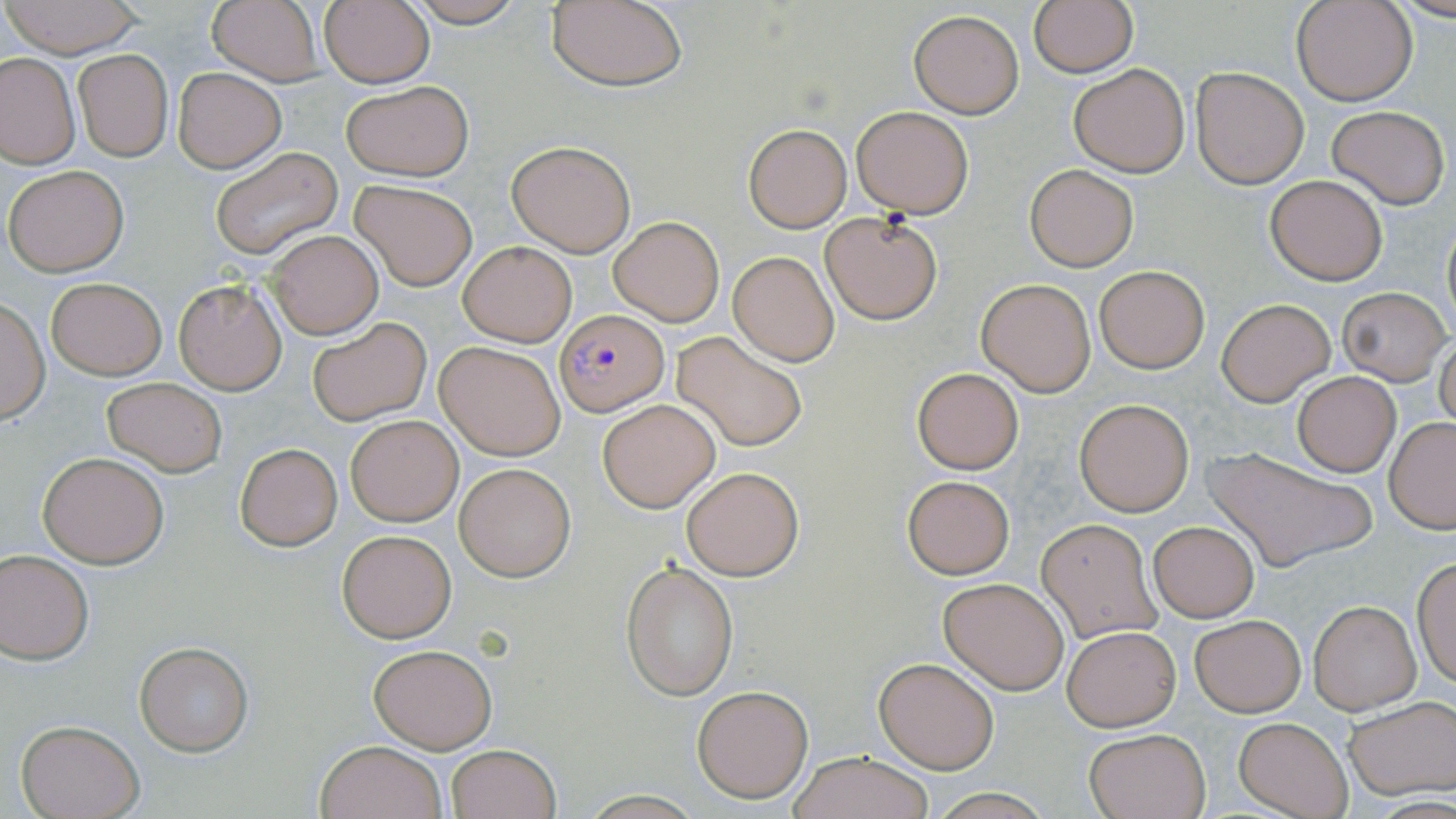
Approximate bounding boxes as named x1/y1/x2/y2 corners in pixels. Plasmodium falciparum-infected red blood cell locations: (x1=555, y1=311, x2=667, y2=417). Uninfected red blood cell locations: (x1=399, y1=0, x2=532, y2=27), (x1=544, y1=0, x2=689, y2=92), (x1=1028, y1=0, x2=1138, y2=78), (x1=1293, y1=0, x2=1417, y2=105), (x1=2, y1=1, x2=147, y2=57), (x1=206, y1=1, x2=324, y2=85), (x1=319, y1=2, x2=434, y2=87), (x1=909, y1=9, x2=1024, y2=119), (x1=74, y1=50, x2=172, y2=161), (x1=0, y1=52, x2=80, y2=169), (x1=1070, y1=64, x2=1190, y2=175), (x1=1189, y1=66, x2=1309, y2=189), (x1=173, y1=68, x2=285, y2=172), (x1=343, y1=80, x2=472, y2=181), (x1=852, y1=105, x2=974, y2=217), (x1=1326, y1=105, x2=1450, y2=209), (x1=742, y1=122, x2=852, y2=232), (x1=506, y1=139, x2=638, y2=256), (x1=210, y1=147, x2=344, y2=261), (x1=4, y1=164, x2=128, y2=277), (x1=1025, y1=164, x2=1138, y2=272), (x1=1265, y1=174, x2=1387, y2=285), (x1=351, y1=182, x2=476, y2=290), (x1=819, y1=213, x2=943, y2=325), (x1=608, y1=214, x2=724, y2=326), (x1=1440, y1=214, x2=1455, y2=340), (x1=268, y1=231, x2=383, y2=340), (x1=458, y1=240, x2=577, y2=347), (x1=728, y1=250, x2=840, y2=365), (x1=1094, y1=266, x2=1208, y2=373), (x1=706, y1=268, x2=829, y2=422), (x1=46, y1=278, x2=166, y2=380), (x1=976, y1=278, x2=1096, y2=396), (x1=174, y1=279, x2=287, y2=394), (x1=1337, y1=287, x2=1452, y2=385), (x1=1216, y1=298, x2=1336, y2=405), (x1=1, y1=299, x2=50, y2=424), (x1=307, y1=318, x2=431, y2=426), (x1=1435, y1=327, x2=1456, y2=434), (x1=672, y1=332, x2=809, y2=453), (x1=435, y1=340, x2=567, y2=460), (x1=912, y1=367, x2=1024, y2=473), (x1=1292, y1=371, x2=1401, y2=475), (x1=103, y1=377, x2=226, y2=477), (x1=1073, y1=397, x2=1196, y2=517), (x1=597, y1=398, x2=721, y2=513), (x1=346, y1=415, x2=462, y2=526), (x1=1384, y1=419, x2=1456, y2=534), (x1=235, y1=443, x2=342, y2=550), (x1=1204, y1=446, x2=1374, y2=570), (x1=38, y1=451, x2=169, y2=568), (x1=454, y1=462, x2=576, y2=582), (x1=681, y1=466, x2=803, y2=580), (x1=902, y1=475, x2=1015, y2=578), (x1=1037, y1=518, x2=1160, y2=642), (x1=1148, y1=520, x2=1259, y2=622), (x1=336, y1=529, x2=457, y2=643), (x1=0, y1=549, x2=95, y2=664), (x1=1412, y1=555, x2=1456, y2=690), (x1=623, y1=562, x2=738, y2=700), (x1=939, y1=576, x2=1071, y2=693), (x1=1309, y1=601, x2=1420, y2=714), (x1=1189, y1=614, x2=1305, y2=717), (x1=1062, y1=625, x2=1182, y2=731), (x1=134, y1=641, x2=253, y2=755), (x1=368, y1=642, x2=497, y2=752), (x1=874, y1=656, x2=999, y2=775), (x1=692, y1=684, x2=814, y2=804), (x1=1345, y1=697, x2=1456, y2=799), (x1=1239, y1=711, x2=1455, y2=805), (x1=1234, y1=718, x2=1352, y2=818), (x1=15, y1=719, x2=145, y2=819), (x1=1084, y1=728, x2=1211, y2=818), (x1=317, y1=740, x2=449, y2=819), (x1=446, y1=744, x2=561, y2=819), (x1=788, y1=750, x2=933, y2=819). Slide-level diagnosis: Plasmodium falciparum. Captured at 1000x magnification. Optical microscopy. May-Grünwald-Giemsa-stained preparation. One field of a larger specimen. Thin blood smear. Image is 1456×819 pixels.